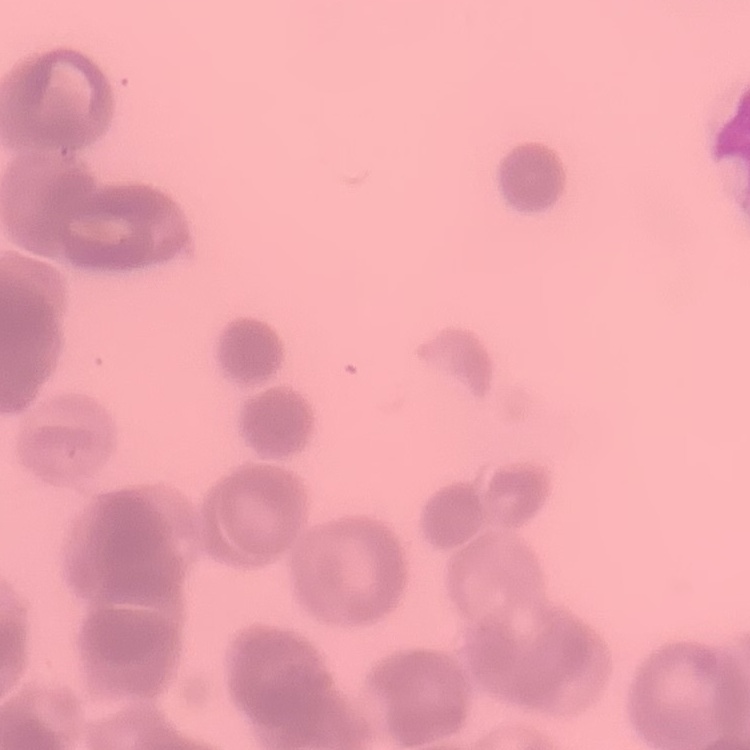

{
  "erythrocyte_morphology": "rouleaux formation",
  "image_type": "one tile cut from a larger photomicrograph",
  "stain": "Field's or Giemsa",
  "preparation": "thin peripheral smear"
}